Report the malaria status of this cell.
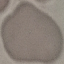
Uninfected.

preparation: thin blood smear
capture: smartphone through the microscope eyepiece
image_type: cell patch, automatically extracted from a larger field of view and resized to 64 × 64 pixels
stain: Giemsa